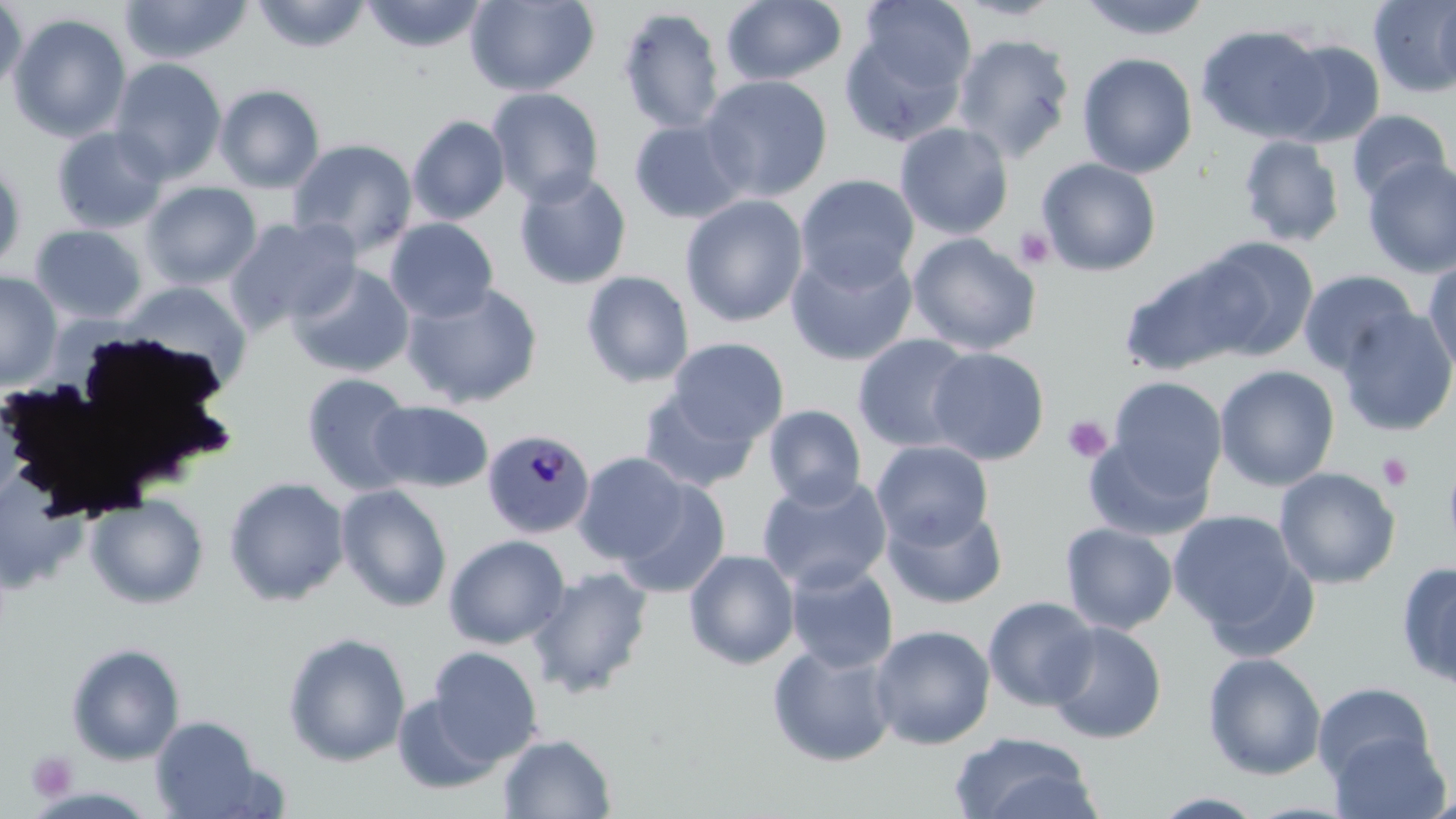

slide-level diagnosis = Plasmodium malariae
preparation = thin blood film
image size = 1456×819 pixels
platelet locations = approximate bounding boxes as (x1,y1)-(x2,y2) corner pairs in pixels: (1014,226)-(1056,270), (1063,416)-(1111,463), (1378,453)-(1413,492), (27,750)-(77,803)
uninfected red blood cell locations = approximate bounding boxes as (x1,y1)-(x2,y2) corner pairs in pixels: (250,0)-(372,53), (465,0)-(600,97), (721,0)-(848,87), (858,0)-(977,94), (951,0)-(1068,22), (1075,0)-(1214,41), (1368,0)-(1456,98), (0,1)-(27,99), (119,1)-(253,65), (361,1)-(489,53), (1434,1)-(1456,93), (617,7)-(725,136), (8,13)-(132,143), (839,23)-(968,147), (1196,24)-(1331,143), (951,33)-(1076,163), (1274,39)-(1386,147), (1076,47)-(1331,165), (1077,52)-(1198,178), (109,58)-(227,183), (700,74)-(833,202), (214,84)-(326,193), (486,87)-(604,207), (1346,109)-(1452,205), (407,115)-(511,225), (629,119)-(750,224), (894,122)-(1014,240), (51,126)-(170,234), (1238,135)-(1346,248), (287,138)-(418,256), (1037,157)-(1162,276), (1362,157)-(1456,278), (0,161)-(27,275), (513,170)-(633,290), (795,174)-(919,291), (140,181)-(262,290), (681,195)-(808,327), (226,216)-(361,332), (385,217)-(499,323), (30,224)-(148,324), (907,232)-(1041,355), (1195,237)-(1319,360), (785,245)-(919,366), (1422,256)-(1456,378), (1120,258)-(1259,377), (287,263)-(415,378), (1298,269)-(1418,376), (580,270)-(695,389), (0,271)-(62,389), (119,281)-(253,389), (401,282)-(544,409), (1336,308)-(1456,437), (852,334)-(978,453), (666,338)-(789,446), (926,347)-(1049,465), (1215,365)-(1340,491), (300,372)-(419,495), (1107,377)-(1227,496), (639,387)-(760,494), (369,400)-(494,493), (763,405)-(867,509), (1083,433)-(1214,541), (871,440)-(994,549), (1442,449)-(1456,561), (573,451)-(690,566), (1274,467)-(1400,589), (756,474)-(893,594), (224,476)-(350,606), (614,478)-(731,598), (336,484)-(453,612), (86,494)-(209,609), (882,503)-(1008,609), (1168,509)-(1311,645), (1060,522)-(1178,636), (444,534)-(570,649), (684,549)-(800,670), (785,562)-(899,673), (1397,562)-(1456,693), (526,566)-(654,698), (983,596)-(1101,711), (1045,621)-(1167,744), (869,625)-(995,750), (282,632)-(412,766), (65,642)-(186,765), (767,642)-(898,768), (427,646)-(543,764), (1203,651)-(1327,780), (1312,682)-(1436,786), (391,691)-(503,794), (151,715)-(266,818), (1329,730)-(1450,819), (950,732)-(1101,819), (498,733)-(617,818), (1149,792)-(1270,818)
stain = May-Grünwald-Giemsa
Plasmodium malariae-infected red blood cell locations = approximate bounding boxes as (x1,y1)-(x2,y2) corner pairs in pixels: (482,428)-(595,540)
magnification = 1000x
field of view = one of a larger specimen
modality = light microscopy